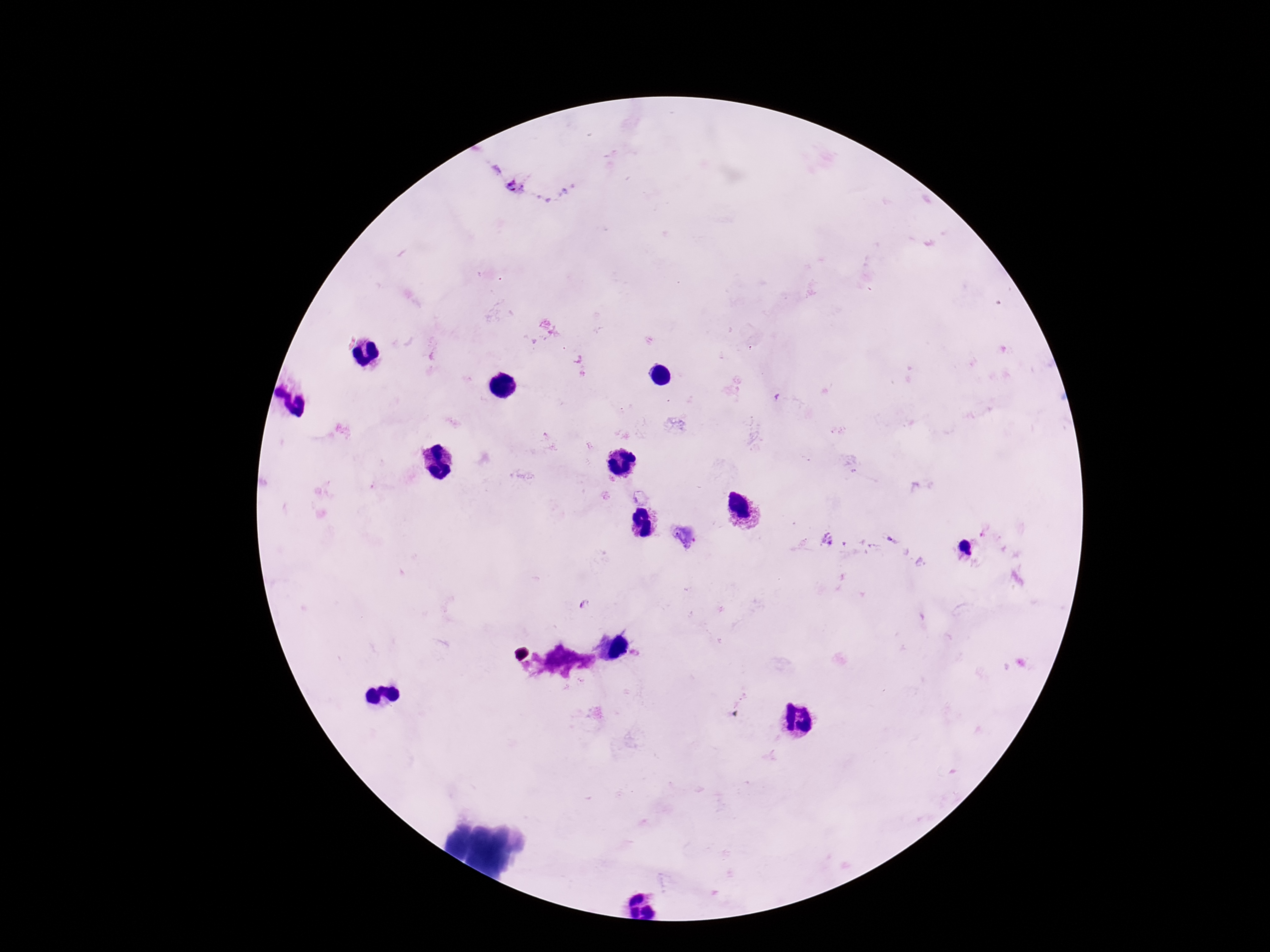

Approximate centers as [x, y] in pixels.
Summary:
  - Plasmodium parasite locations: [515, 187], [889, 538], [969, 555]
  - Field of view: single
  - Preparation: thick blood smear
  - Capture: smartphone camera through the microscope eyepiece
  - Image size: 1270×952 pixels
  - Stain: Giemsa
  - Patient malaria status: positive
  - Magnification: 100x